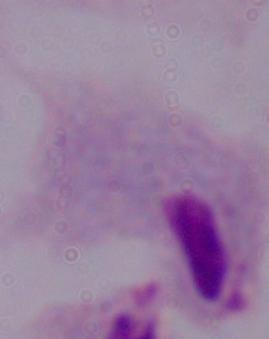

Summary:
  - Magnification: 1000x
  - Modality: micrograph
  - Identification: trichomonad